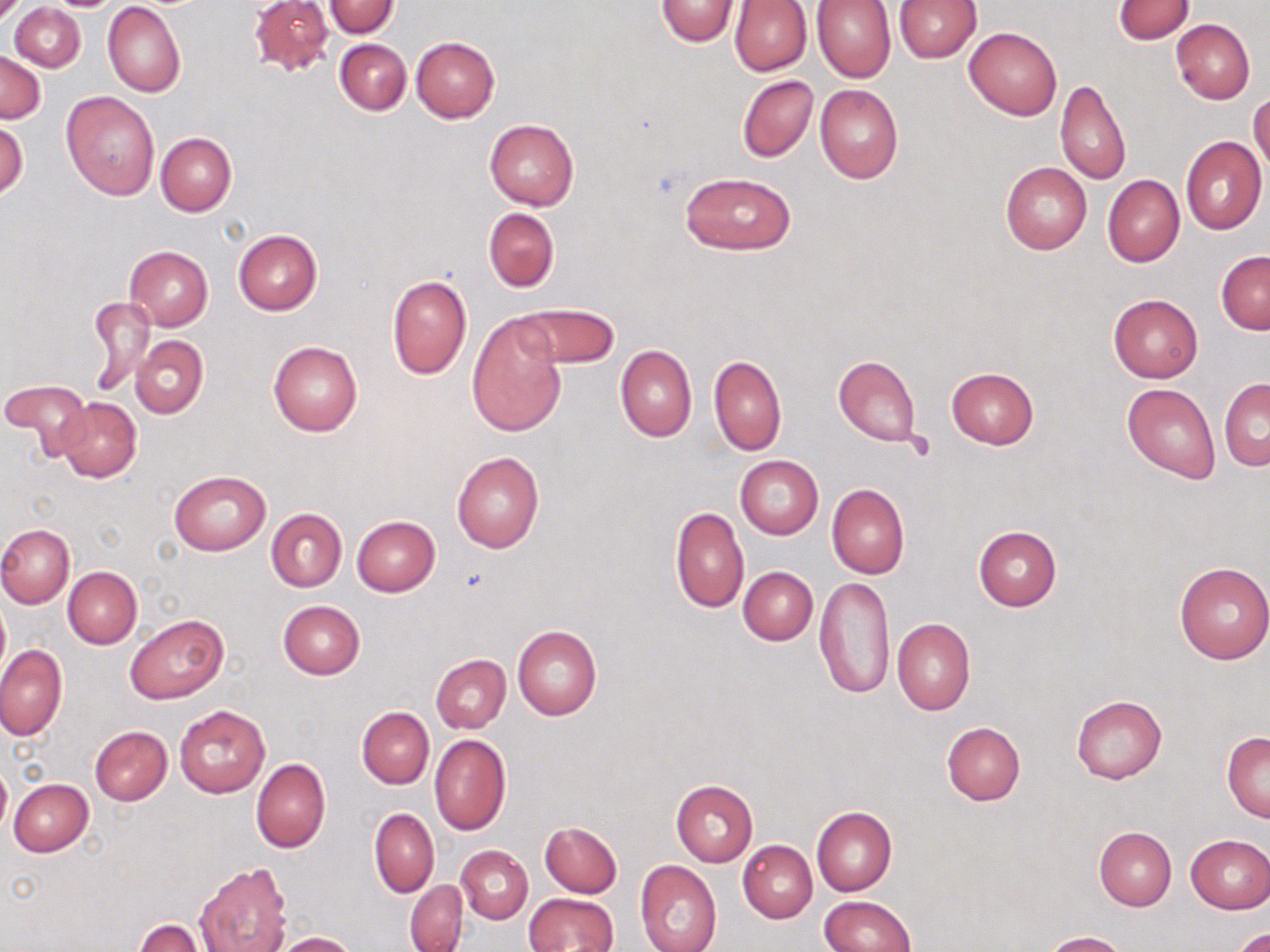

Summary:
  - Coordinate format: approximate bounding boxes as [x1, y1, x2, y2] in pixels
  - Uninfected red blood cell locations: [249, 0, 333, 76], [656, 0, 740, 45], [895, 0, 981, 62], [729, 1, 811, 75], [812, 1, 896, 84], [1112, 1, 1194, 45], [10, 2, 85, 72], [103, 2, 185, 98], [325, 2, 399, 38], [1172, 18, 1255, 104], [964, 26, 1062, 120], [411, 36, 500, 123], [334, 38, 411, 115], [1, 51, 45, 123], [737, 75, 818, 163], [1056, 79, 1130, 186], [816, 83, 903, 183], [62, 91, 160, 200], [1249, 93, 1270, 174], [484, 117, 579, 211], [0, 118, 28, 202], [155, 132, 236, 216], [1181, 137, 1267, 235], [1000, 162, 1091, 254], [680, 172, 794, 254], [1101, 175, 1185, 267], [483, 207, 559, 292], [233, 229, 322, 315], [124, 246, 213, 331], [1216, 251, 1270, 335], [387, 274, 472, 380], [1108, 294, 1203, 382], [85, 295, 155, 398], [520, 300, 620, 367], [467, 313, 567, 438], [131, 336, 208, 418], [268, 340, 362, 436], [616, 344, 696, 442], [709, 355, 787, 456], [833, 355, 921, 446], [946, 367, 1040, 448], [1219, 378, 1269, 470], [1, 379, 90, 461], [1122, 383, 1219, 483], [55, 397, 141, 482], [451, 451, 545, 554], [735, 456, 823, 539], [169, 469, 271, 556], [827, 484, 909, 579], [669, 507, 749, 612], [266, 508, 347, 592], [352, 515, 441, 596], [0, 524, 74, 607], [973, 526, 1061, 610], [1174, 561, 1269, 665], [63, 566, 142, 648], [738, 566, 818, 646], [815, 576, 894, 699], [0, 599, 9, 675], [277, 601, 364, 679], [126, 615, 228, 705], [892, 618, 975, 714], [513, 624, 602, 720], [0, 645, 67, 740], [431, 655, 510, 732], [1071, 693, 1167, 784], [175, 705, 269, 797], [357, 707, 434, 788], [941, 722, 1025, 806], [90, 726, 172, 805], [1222, 732, 1270, 821], [429, 733, 511, 836], [251, 758, 330, 853], [0, 761, 11, 835], [9, 779, 93, 856], [671, 780, 759, 866], [811, 808, 896, 896], [369, 809, 439, 897], [540, 822, 622, 897], [1094, 826, 1177, 910], [1185, 834, 1269, 914], [738, 840, 817, 923], [458, 845, 533, 922], [635, 860, 721, 952], [195, 861, 293, 952], [404, 880, 468, 952], [523, 893, 618, 952], [820, 896, 915, 952], [134, 918, 202, 952], [1232, 927, 1269, 952], [270, 931, 358, 952], [1041, 931, 1126, 952]
  - Slide-level diagnosis: negative for blood parasites
  - Preparation: thin blood film
  - Modality: light microscopy
  - Stain: May-Grünwald-Giemsa
  - Image size: 1270×952 pixels
  - Field of view: single
  - Magnification: 1000x